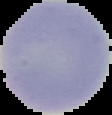
preparation = thin blood film
image type = segmented cell region with the area outside set to black
malaria status = uninfected
image size = 112×115 pixels